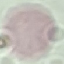
result = no malaria parasites detected
capture = smartphone through the microscope eyepiece
preparation = thin smear
image type = cell patch, automatically extracted from a larger field of view and resized to 64 × 64 pixels
stain = Giemsa